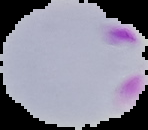
Summary:
  - Preparation: thin blood smear
  - Malaria status: parasitized
  - Image type: segmented cell region with the area outside set to black
  - Image size: 148×130 pixels